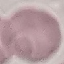

Summary:
  - Result: no malaria parasites detected
  - Stain: Giemsa
  - Capture: smartphone camera at the microscope eyepiece
  - Preparation: thin smear
  - Image type: automatically extracted cell patch, resized to 64 × 64 pixels